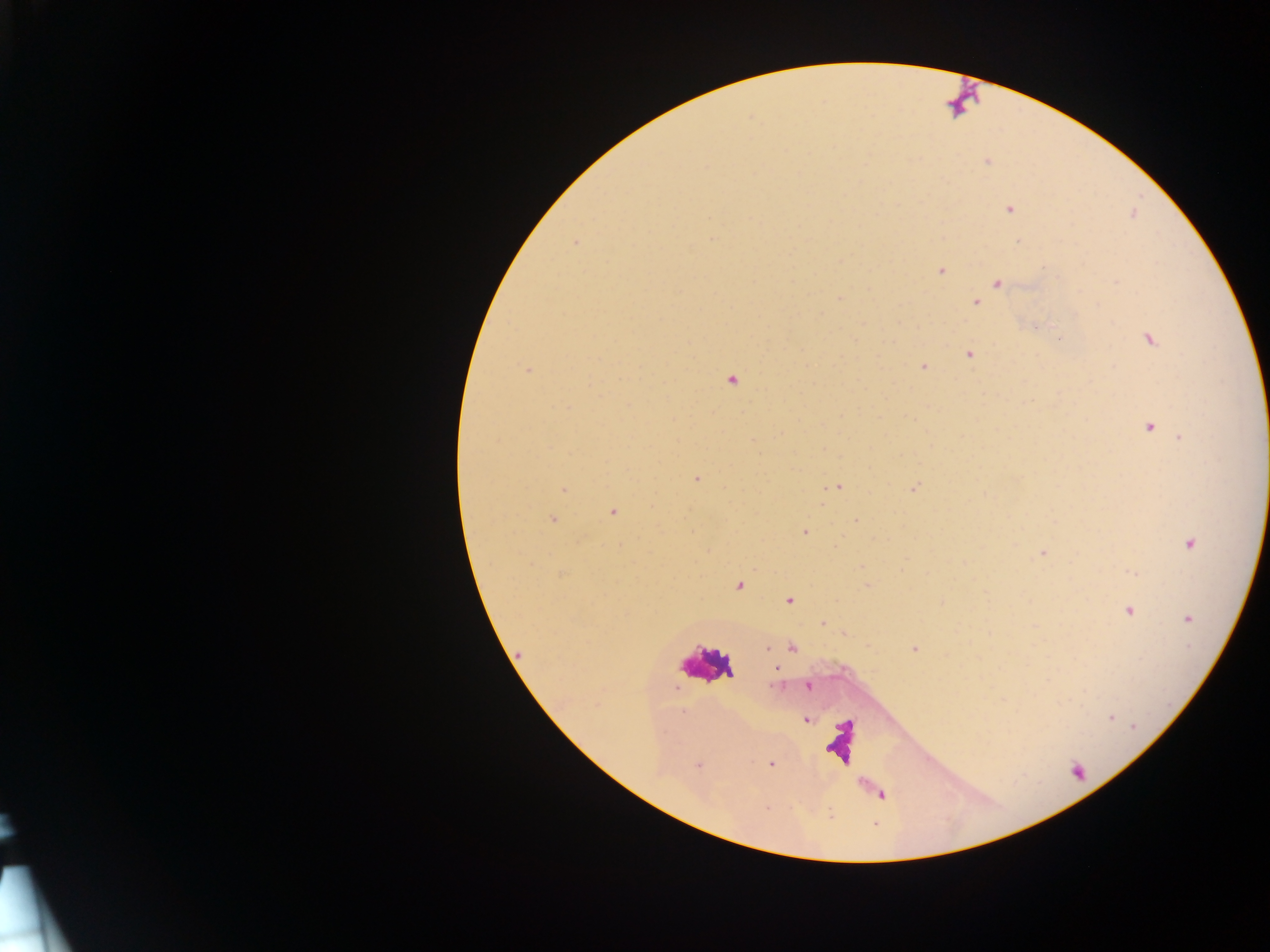 Approximate centers as [x, y] in pixels. Malaria parasite locations: [987, 161], [1010, 209], [713, 239], [575, 243], [940, 271], [997, 282], [839, 298], [976, 303], [1149, 339], [969, 354], [923, 367], [526, 370], [731, 381], [1149, 427], [1180, 437], [697, 479], [837, 486], [914, 488], [564, 490], [613, 512], [552, 519], [856, 521], [805, 532], [1190, 544], [1043, 553], [1132, 572], [739, 586], [790, 600], [1128, 611], [1188, 619], [822, 622], [792, 647], [768, 648], [915, 649], [777, 669], [808, 686], [1111, 718], [807, 720], [1134, 726], [771, 764], [698, 765]. Leukocyte locations: [702, 663]. One field of view. Image is 1270×952 pixels. Collected in Ghana. Mobile-phone photograph taken through the microscope. Thick blood smear.